Classify this cell by malaria status.
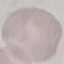
It is uninfected.

Cell patch, automatically extracted from a larger field of view and resized to 64 × 64 pixels. Acquired by smartphone through the microscope eyepiece. Giemsa stain. Thin blood smear.